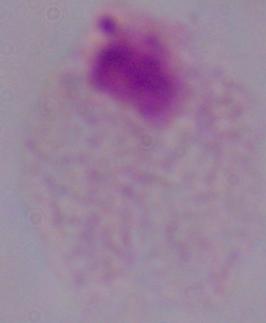

Summary:
  - Modality: photomicrograph
  - Magnification: 1000x
  - Identification: trichomonad